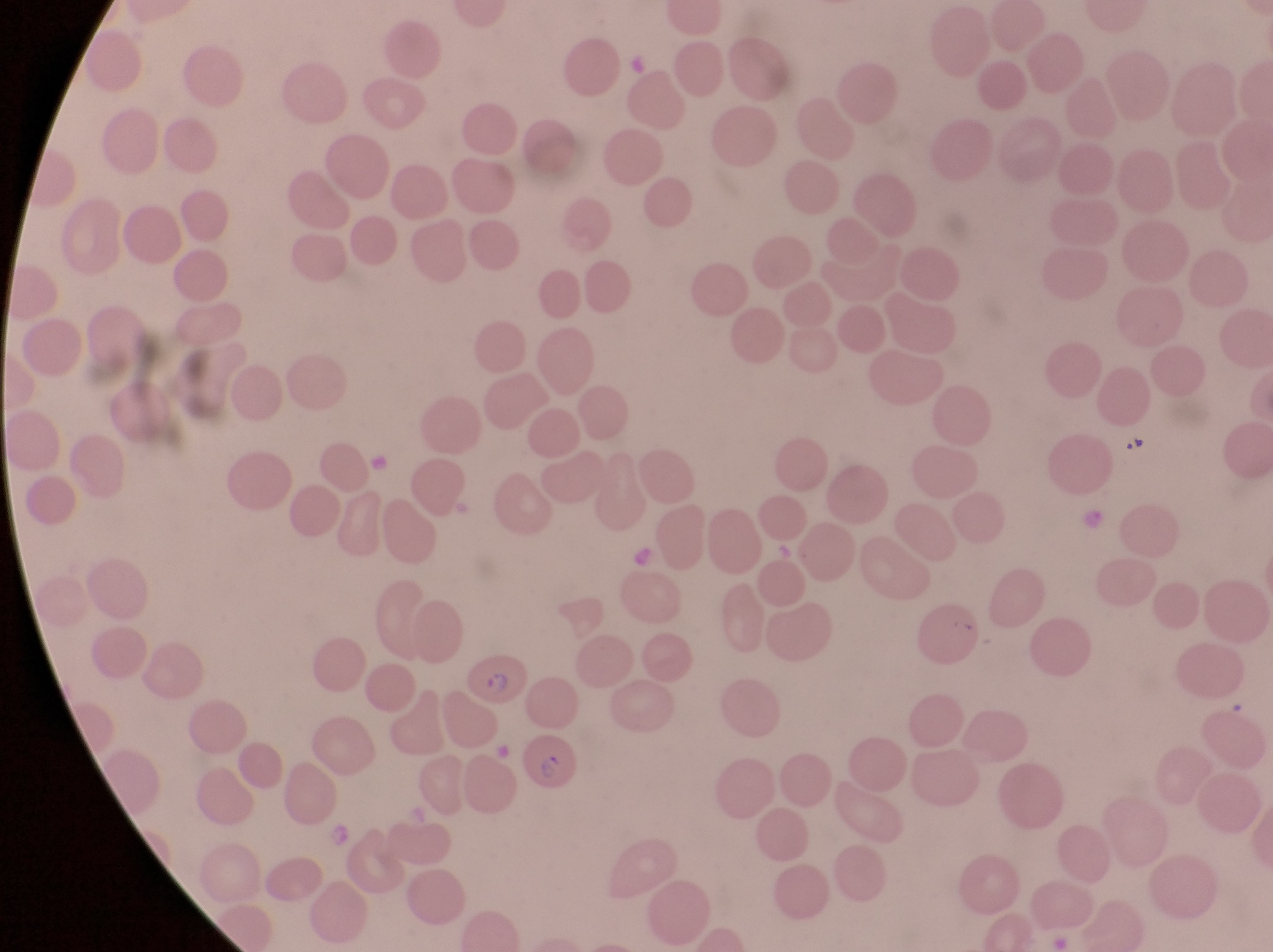
Approximate bounding boxes as [left, top, right, bottom] in pixels. Parasitised red blood cell locations: [457, 651, 531, 711], [521, 729, 584, 799]. Captured by a smartphone held over the eyepiece of an Olympus CX-23 microscope. At a magnification of 1000x. Sample from Uganda. Image is 1273×952 pixels. Single field of view. Thin blood smear.